Report the malaria status of this cell.
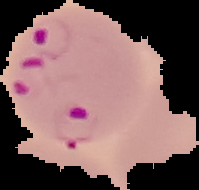

Parasitized.

image_type: segmented cell region on a black background
preparation: thin blood film
image_size: 199×190 pixels